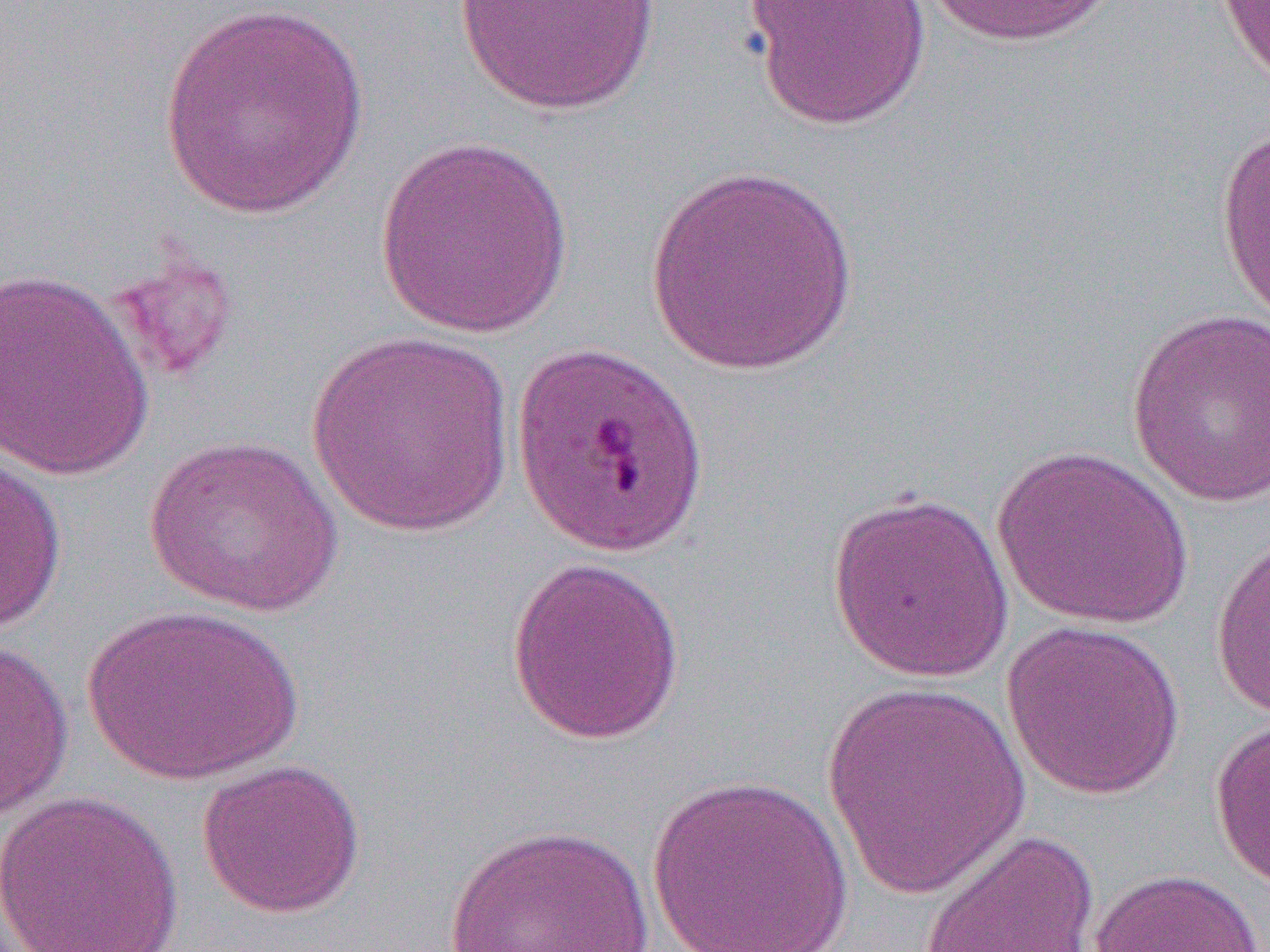

slide-level diagnosis = Plasmodium falciparum
field of view = one of a larger specimen
modality = light microscopy
image size = 1270×952 pixels
magnification = 1000x
preparation = thin blood film
uninfected red blood cell locations = approximate bounding boxes as named x1/y1/x2/y2 corners in pixels: (x1=451, y1=0, x2=661, y2=116), (x1=741, y1=0, x2=934, y2=131), (x1=924, y1=0, x2=1122, y2=48), (x1=1216, y1=0, x2=1270, y2=88), (x1=156, y1=2, x2=372, y2=221), (x1=1216, y1=123, x2=1270, y2=331), (x1=372, y1=136, x2=573, y2=338), (x1=643, y1=165, x2=861, y2=375), (x1=104, y1=248, x2=241, y2=385), (x1=0, y1=267, x2=155, y2=481), (x1=1126, y1=307, x2=1270, y2=509), (x1=305, y1=331, x2=516, y2=538), (x1=144, y1=434, x2=345, y2=617), (x1=992, y1=444, x2=1194, y2=630), (x1=0, y1=453, x2=67, y2=636), (x1=826, y1=488, x2=1015, y2=683), (x1=1210, y1=531, x2=1269, y2=724), (x1=506, y1=555, x2=687, y2=745), (x1=82, y1=604, x2=304, y2=787), (x1=1000, y1=619, x2=1186, y2=800), (x1=0, y1=632, x2=75, y2=823), (x1=819, y1=682, x2=1034, y2=899), (x1=1209, y1=715, x2=1270, y2=898), (x1=196, y1=758, x2=366, y2=919), (x1=646, y1=773, x2=854, y2=951), (x1=0, y1=789, x2=185, y2=952), (x1=442, y1=823, x2=656, y2=951), (x1=918, y1=827, x2=1099, y2=952), (x1=1086, y1=867, x2=1264, y2=952)